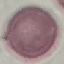
Result: negative for malaria parasites. Giemsa-stained preparation. Thin blood film. Automatically extracted cell patch, resized to 64 × 64 pixels. Photographed with a smartphone camera at the microscope eyepiece.